Classify this cell by malaria status.
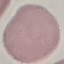

Uninfected.

Cell patch, automatically extracted from a larger field of view and resized to 64 × 64 pixels. Giemsa stain. Photographed with a smartphone camera at the microscope eyepiece. Thin blood smear.